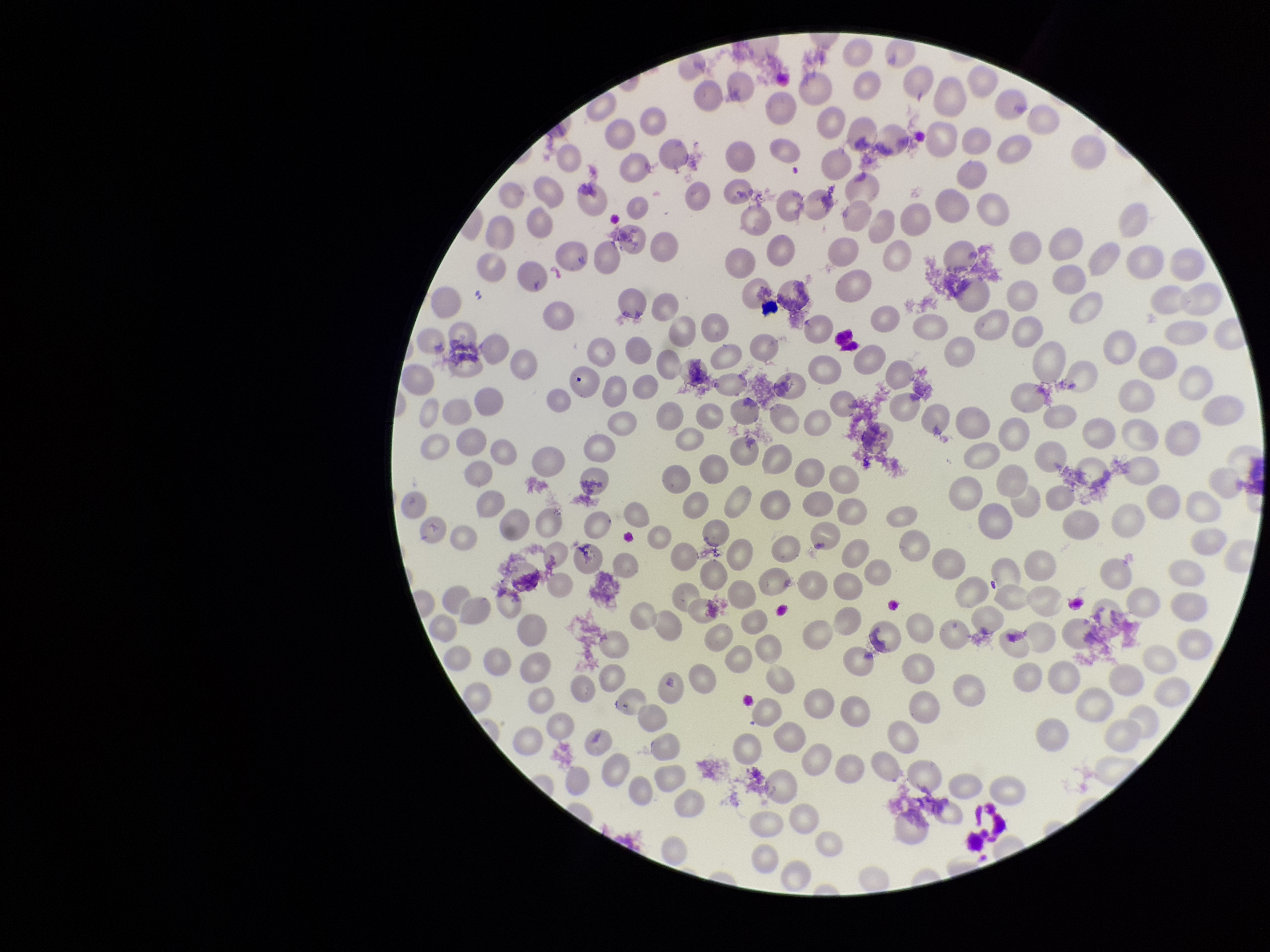 One field from this slide. Patient malaria status: negative. Preparation: thin smear. Giemsa stain. Smartphone photograph taken through the eyepiece of a microscope. Parasitized red blood cells: none detected. Image is 1270×952 pixels. Red blood cell count: 245. Parasitized red blood cell count: 0.